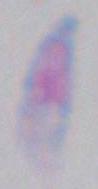
magnification = 1000x
modality = micrograph
identification = Toxoplasma gondii